Assess this cell for malaria.
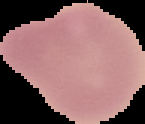
It is uninfected.

Summary:
  - Image type: segmented cell region with the area outside set to black
  - Image size: 145×124 pixels
  - Preparation: thin blood smear